Assess this cell for malaria.
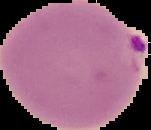

Parasitized.

Summary:
  - Image type: segmented cell region with the area outside set to black
  - Image size: 151×130 pixels
  - Preparation: thin blood film